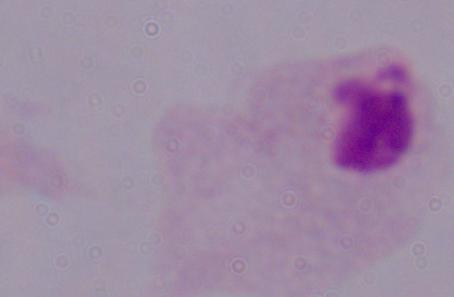
Summary:
  - Magnification: 1000x
  - Modality: micrograph
  - Identification: trichomonad